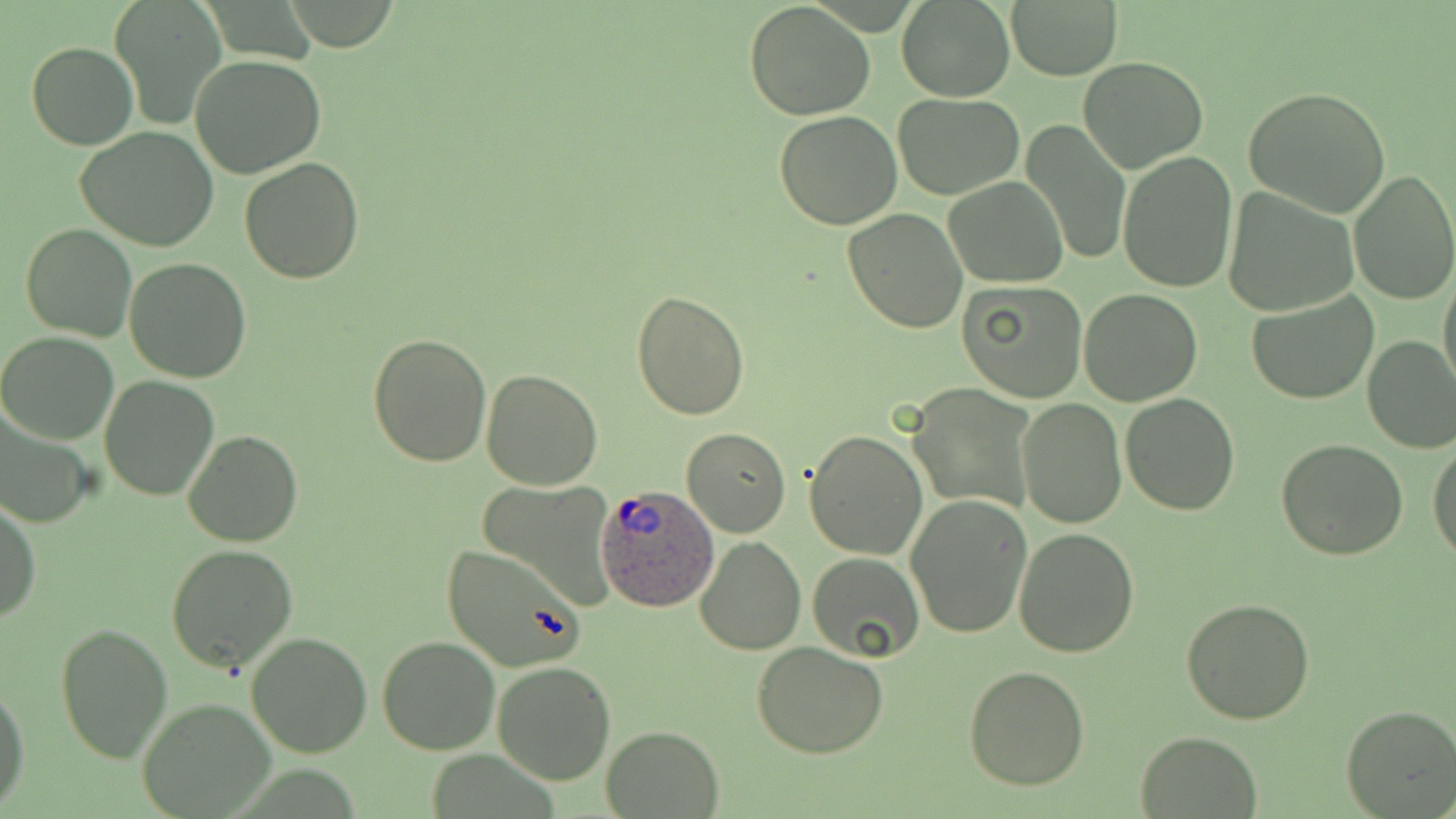
Summary:
  - Coordinate format: approximate bounding boxes as named x1/y1/x2/y2 corners in pixels
  - Plasmodium ovale-infected red blood cell locations: (x1=594, y1=482, x2=719, y2=614)
  - Uninfected red blood cell locations: (x1=108, y1=0, x2=225, y2=127), (x1=745, y1=1, x2=875, y2=119), (x1=897, y1=2, x2=1015, y2=102), (x1=1007, y1=2, x2=1121, y2=80), (x1=26, y1=41, x2=138, y2=150), (x1=191, y1=53, x2=326, y2=176), (x1=1078, y1=56, x2=1208, y2=173), (x1=1243, y1=87, x2=1392, y2=218), (x1=893, y1=91, x2=1024, y2=199), (x1=773, y1=110, x2=904, y2=230), (x1=1018, y1=120, x2=1130, y2=264), (x1=76, y1=126, x2=219, y2=250), (x1=1117, y1=150, x2=1239, y2=294), (x1=240, y1=158, x2=364, y2=282), (x1=1348, y1=168, x2=1456, y2=305), (x1=944, y1=176, x2=1068, y2=287), (x1=1223, y1=187, x2=1360, y2=318), (x1=842, y1=207, x2=968, y2=334), (x1=21, y1=223, x2=137, y2=342), (x1=124, y1=258, x2=252, y2=384), (x1=1438, y1=266, x2=1455, y2=399), (x1=957, y1=279, x2=1088, y2=404), (x1=1078, y1=288, x2=1202, y2=406), (x1=630, y1=290, x2=750, y2=421), (x1=1247, y1=290, x2=1379, y2=405), (x1=1, y1=331, x2=119, y2=444), (x1=367, y1=333, x2=492, y2=467), (x1=1362, y1=336, x2=1456, y2=454), (x1=479, y1=369, x2=603, y2=490), (x1=100, y1=375, x2=218, y2=502), (x1=907, y1=385, x2=1037, y2=516), (x1=1120, y1=392, x2=1239, y2=514), (x1=1017, y1=399, x2=1126, y2=529), (x1=0, y1=401, x2=97, y2=530), (x1=682, y1=428, x2=790, y2=538), (x1=804, y1=429, x2=928, y2=560), (x1=184, y1=430, x2=303, y2=548), (x1=1276, y1=437, x2=1408, y2=558), (x1=1429, y1=437, x2=1456, y2=562), (x1=477, y1=481, x2=619, y2=607), (x1=906, y1=492, x2=1035, y2=638), (x1=1, y1=499, x2=40, y2=628), (x1=1013, y1=527, x2=1140, y2=658), (x1=694, y1=537, x2=806, y2=657), (x1=165, y1=542, x2=300, y2=673), (x1=440, y1=543, x2=586, y2=673), (x1=807, y1=551, x2=925, y2=663), (x1=1181, y1=596, x2=1316, y2=724), (x1=56, y1=622, x2=173, y2=763), (x1=246, y1=631, x2=374, y2=757), (x1=376, y1=636, x2=502, y2=755), (x1=750, y1=640, x2=890, y2=759), (x1=492, y1=662, x2=617, y2=784), (x1=964, y1=666, x2=1089, y2=790), (x1=0, y1=682, x2=29, y2=809), (x1=136, y1=697, x2=278, y2=819), (x1=1340, y1=705, x2=1456, y2=818), (x1=601, y1=725, x2=724, y2=817), (x1=1135, y1=731, x2=1261, y2=817)
  - Slide-level diagnosis: Plasmodium ovale
  - Field of view: single
  - Preparation: thin blood smear
  - Stain: May-Grünwald-Giemsa
  - Modality: optical microscopy
  - Magnification: 1000x
  - Image size: 1456×819 pixels